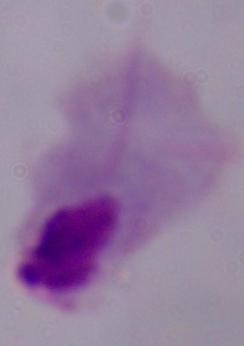

{
  "modality": "photomicrograph",
  "identification": "trichomonad",
  "magnification": "1000x"
}